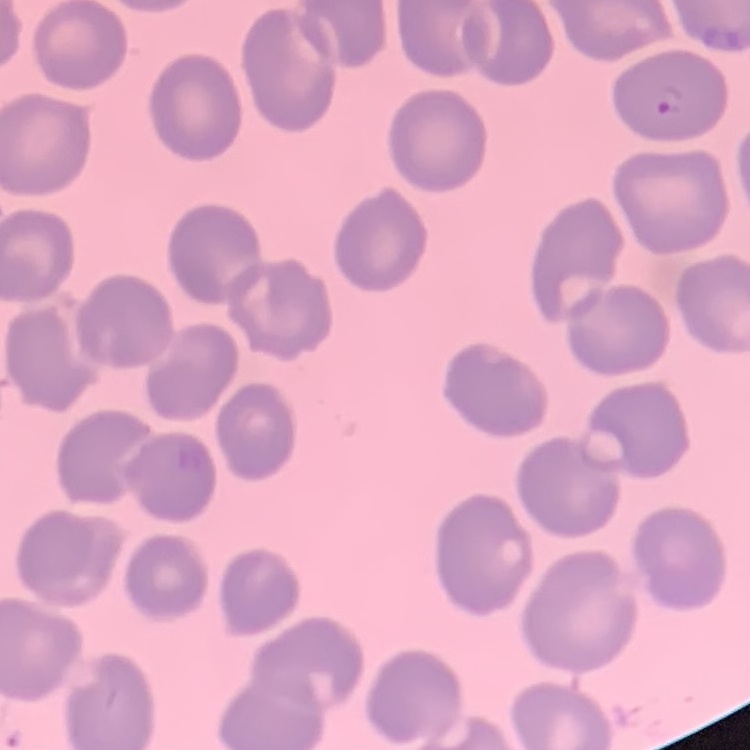
The erythrocytes show no rouleaux formation. Thin peripheral smear. One tile cut from a larger photomicrograph. Stained with either Field's or Giemsa.